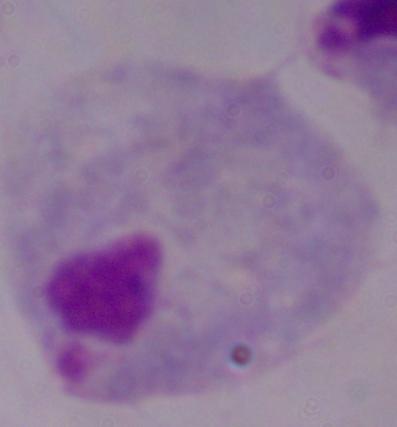

magnification = 1000x
identification = trichomonad
modality = photomicrograph